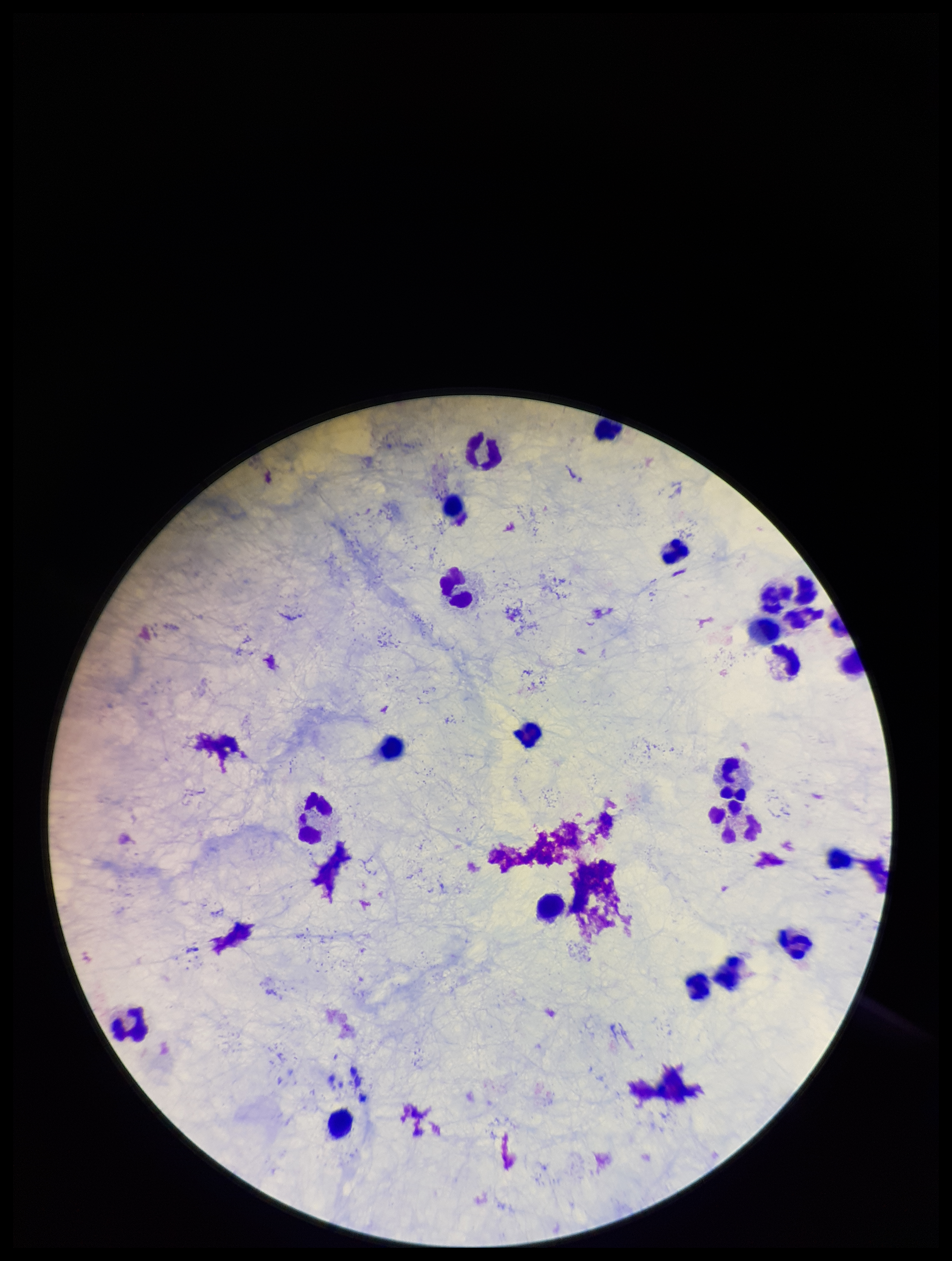

Parasite count: 0. Photographed through the microscope eyepiece with a smartphone camera. Leukocyte count: 21. Giemsa stain. Plasmodium parasites: none identified. Preparation: thick blood smear. Patient malaria status: negative. Single field of view. Image is 952×1261 pixels.